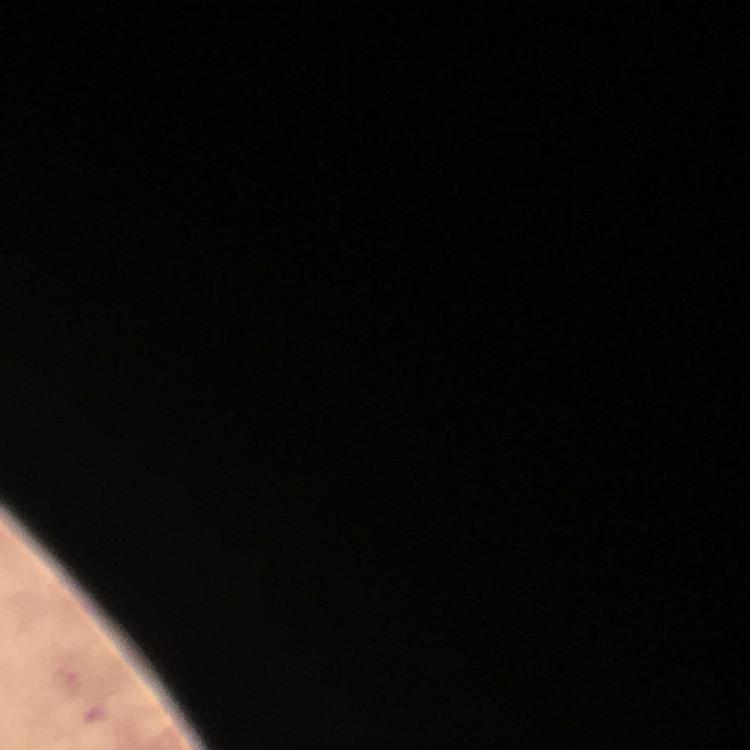 Approximate object centers, in pixels from the top-left corner. Malaria parasite locations: (x=67, y=684), (x=95, y=713). Giemsa-stained preparation. From a diagnostic examination for malaria. Thick blood smear. Immersion oil applied. Image is 750×750 pixels. Smartphone photograph taken through a microscope. Cropped region of a single field of view. 100x magnification.